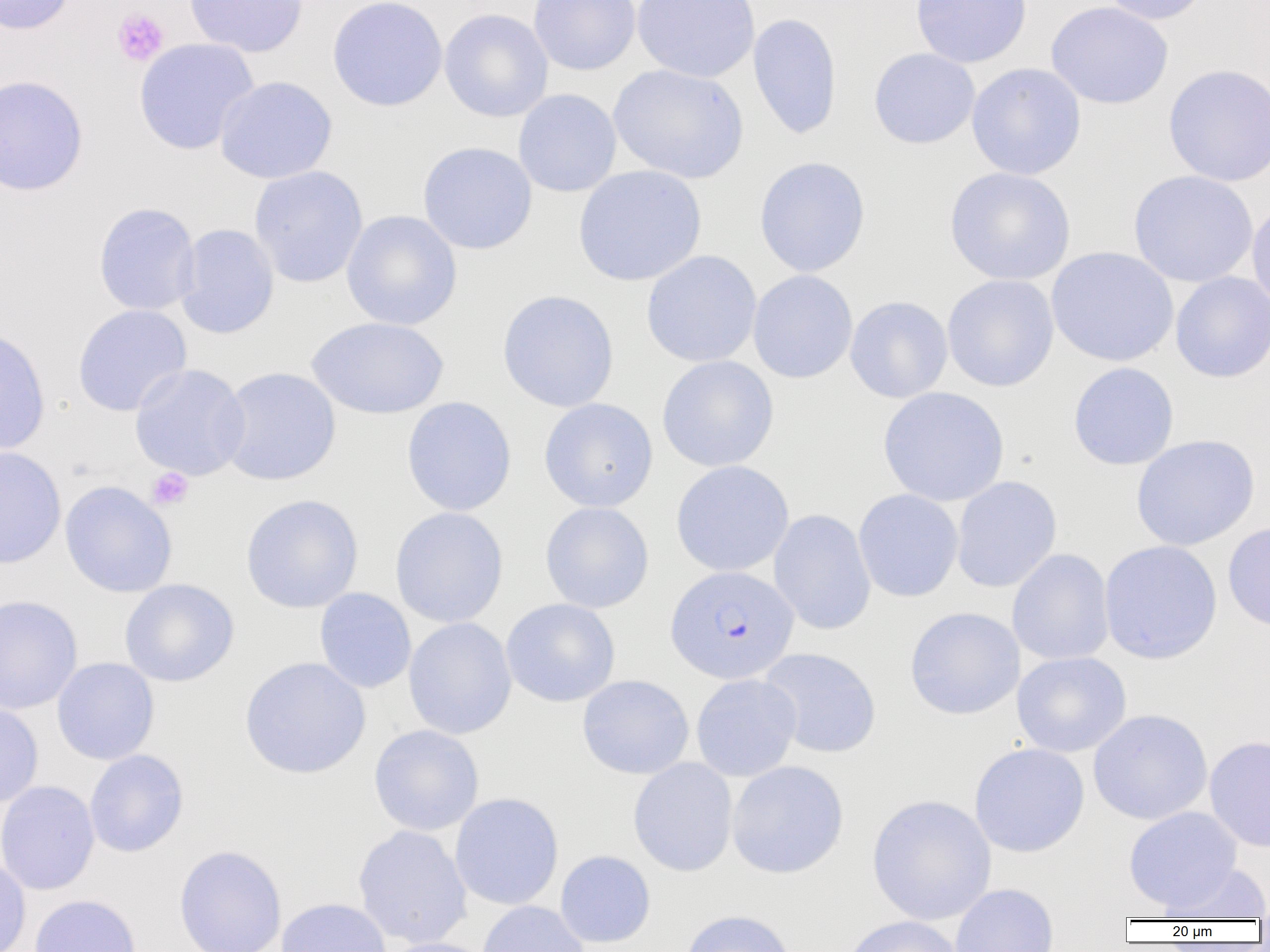
Approximate bounding boxes as [x1, y1, x2, y2] in pixels. Uninfected red blood cell locations: [0, 0, 76, 35], [184, 0, 308, 57], [326, 0, 448, 111], [528, 0, 641, 76], [632, 0, 760, 83], [910, 0, 1032, 68], [1098, 0, 1211, 25], [1046, 2, 1174, 110], [439, 8, 553, 123], [748, 12, 842, 140], [134, 38, 259, 155], [868, 48, 980, 149], [966, 62, 1087, 180], [608, 64, 748, 184], [1163, 64, 1270, 186], [0, 74, 89, 196], [215, 75, 338, 184], [513, 88, 622, 198], [417, 142, 538, 255], [754, 156, 871, 277], [248, 165, 369, 288], [573, 165, 706, 287], [945, 167, 1075, 286], [1128, 170, 1258, 288], [1246, 198, 1270, 313], [93, 202, 201, 315], [341, 210, 463, 331], [175, 223, 280, 339], [1046, 247, 1179, 367], [641, 250, 762, 368], [747, 270, 858, 383], [1170, 272, 1270, 383], [942, 274, 1059, 392], [497, 289, 619, 413], [845, 295, 953, 404], [72, 304, 192, 416], [307, 316, 449, 420], [0, 326, 51, 455], [657, 355, 779, 473], [1067, 362, 1180, 470], [129, 363, 250, 481], [217, 367, 341, 487], [877, 386, 1009, 507], [401, 396, 517, 516], [538, 397, 659, 512], [1131, 435, 1260, 551], [0, 446, 66, 569], [670, 460, 794, 577], [951, 475, 1062, 592], [60, 480, 178, 598], [853, 489, 964, 603], [240, 494, 364, 614], [540, 502, 654, 613], [389, 506, 509, 628], [768, 509, 876, 635], [1222, 521, 1270, 632], [1098, 540, 1223, 664], [1007, 548, 1114, 666], [119, 579, 239, 687], [314, 588, 416, 693], [0, 594, 83, 714], [501, 598, 621, 707], [904, 606, 1025, 720], [403, 617, 517, 740], [758, 647, 882, 758], [1011, 651, 1131, 758], [52, 657, 160, 765], [239, 657, 371, 779], [691, 673, 802, 782], [577, 674, 694, 780], [0, 700, 44, 808], [1088, 708, 1213, 825], [368, 724, 484, 836], [1204, 735, 1270, 853], [969, 743, 1090, 858], [84, 749, 189, 857], [628, 757, 738, 877], [726, 760, 849, 879], [0, 780, 100, 896], [450, 792, 564, 910], [866, 793, 997, 925], [1123, 806, 1242, 912], [352, 825, 472, 949], [174, 844, 287, 952], [555, 850, 656, 947], [0, 856, 31, 952], [1157, 863, 1270, 921], [949, 883, 1059, 952], [29, 894, 142, 952], [276, 897, 392, 952], [477, 901, 590, 952], [680, 909, 797, 952], [841, 915, 966, 952], [379, 937, 496, 952]. Platelet locations: [112, 7, 169, 66], [147, 467, 194, 511]. Plasmodium falciparum-infected red blood cell locations: [666, 566, 799, 684]. Slide-level diagnosis: Plasmodium falciparum. 1000x magnification. Single field of view. Image is 1270×952 pixels. Light microscopy. Thin blood film.